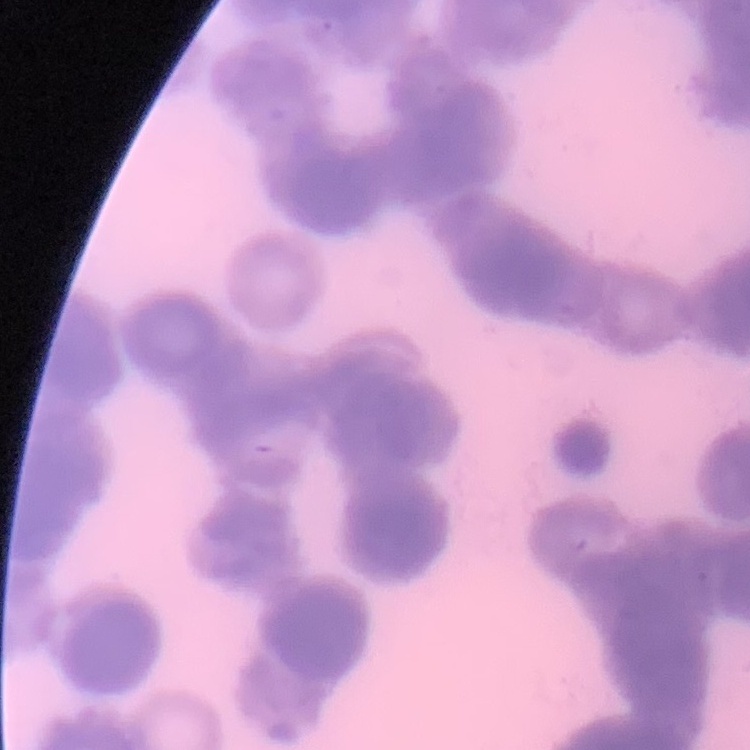
{
  "red_blood_cell_morphology": "rouleaux formation",
  "stain": "Field's or Giemsa",
  "preparation": "thin blood smear",
  "image_type": "square crop of a larger photomicrograph"
}